State which parasite is depicted.
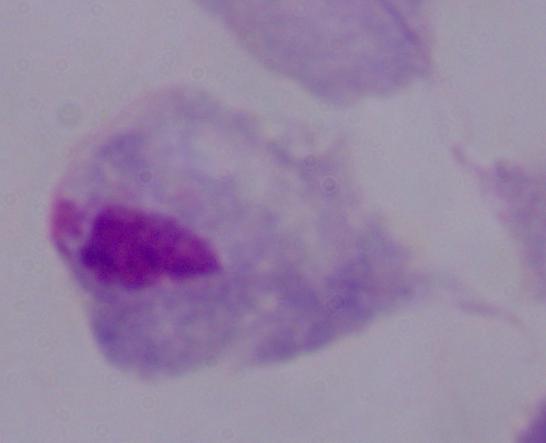

This is a trichomonad.

modality = photomicrograph
magnification = 1000x